Locate and identify every blood parasite.
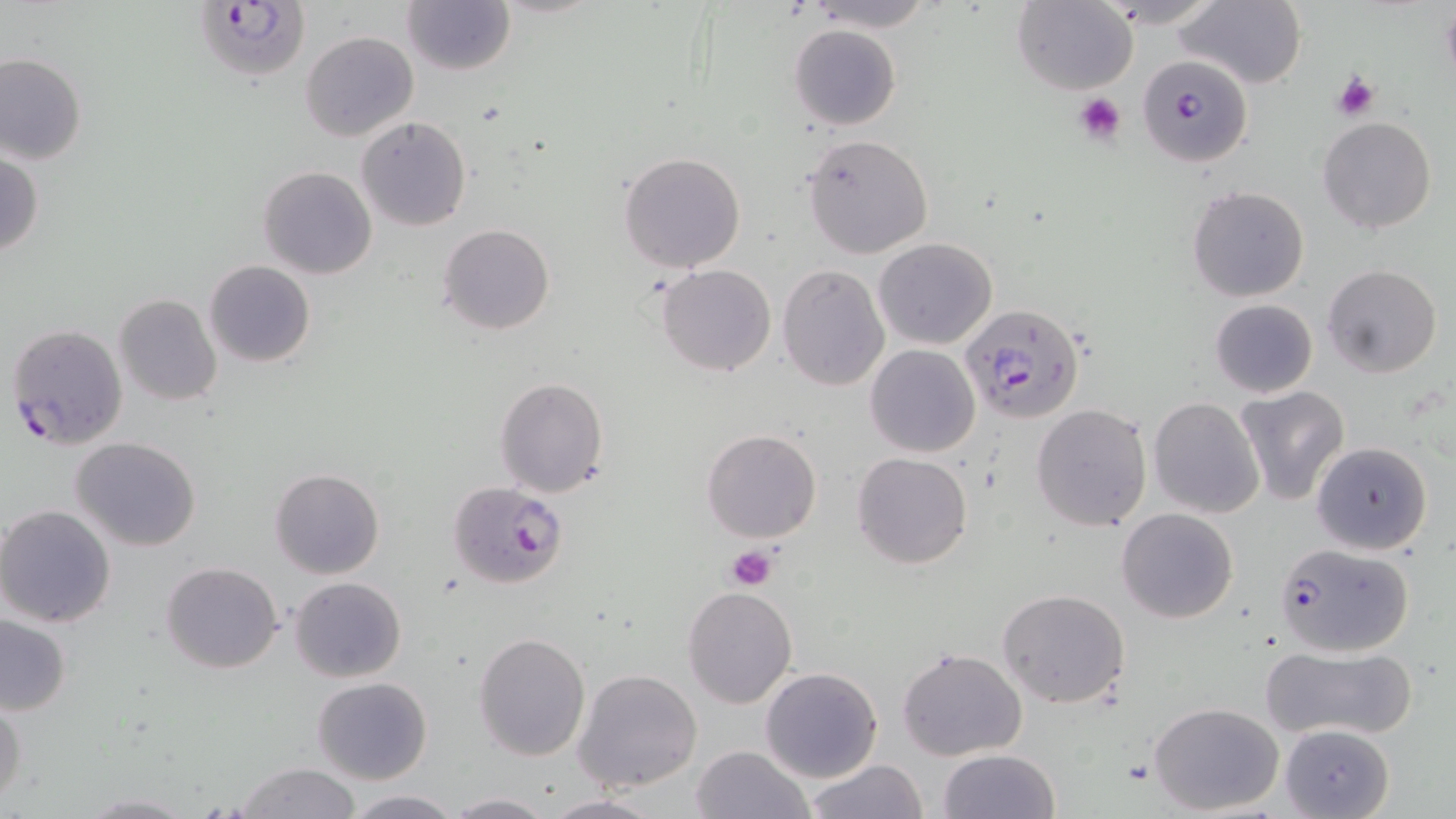
Approximate bounding boxes as (x1,y1)-(x2,y2) corner pairs in pixels.
Plasmodium falciparum-infected red blood cells: (193,0)-(311,84), (1144,64)-(1251,174), (960,302)-(1085,424), (5,322)-(128,451), (445,481)-(568,589), (1273,542)-(1414,657).
No Plasmodium ovale, Plasmodium malariae, Plasmodium vivax, Babesia divergens, or Trypanosoma brucei observed.

Platelet locations: (1331,72)-(1380,121), (1073,92)-(1125,146), (726,545)-(776,591). Uninfected red blood cell locations: (803,0)-(938,30), (1176,0)-(1308,89), (404,1)-(515,76), (1012,2)-(1138,94), (790,24)-(901,130), (300,32)-(418,142), (0,53)-(87,166), (355,116)-(471,233), (1318,117)-(1437,235), (801,133)-(933,258), (1,148)-(43,259), (618,152)-(747,273), (259,165)-(377,280), (1187,186)-(1310,300), (439,223)-(554,335), (873,237)-(998,350), (205,261)-(316,367), (659,263)-(776,377), (775,263)-(889,392), (1321,264)-(1442,379), (113,293)-(224,407), (1209,299)-(1318,397), (865,344)-(979,457), (494,376)-(609,497), (1234,385)-(1350,506), (1148,397)-(1264,519), (1031,404)-(1151,533), (701,427)-(823,544), (71,436)-(202,551), (1310,441)-(1432,555), (852,453)-(972,570), (270,466)-(385,579), (0,504)-(119,627), (1117,507)-(1238,623), (161,563)-(283,674), (289,576)-(406,681), (681,586)-(797,708), (997,589)-(1131,710), (2,616)-(71,714), (473,632)-(592,761), (1261,644)-(1418,742), (897,646)-(1027,760), (760,667)-(884,783), (573,668)-(703,792), (312,676)-(433,784), (0,695)-(27,806), (1149,701)-(1284,816), (1280,724)-(1393,817), (689,745)-(813,819), (937,749)-(1059,819), (804,759)-(929,818), (236,762)-(363,819), (342,791)-(461,818), (77,792)-(197,818), (444,792)-(556,817), (543,792)-(666,818). Slide-level diagnosis: Plasmodium falciparum. May-Grünwald-Giemsa-stained preparation. 1000x magnification. Thin blood smear. Image is 1456×819 pixels. Single field of view. Optical microscopy.